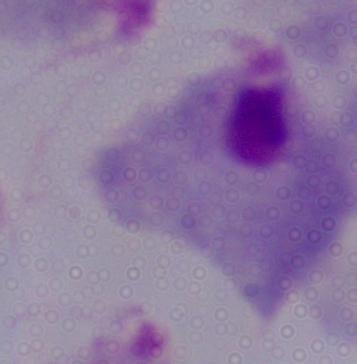
Photomicrograph. A trichomonad is seen. Captured at 1000x magnification.